Report the malaria status of this cell.
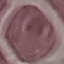
Uninfected.

{
  "stain": "Giemsa",
  "capture": "smartphone through the microscope eyepiece",
  "image_type": "cell patch, automatically extracted from a larger field of view and resized to 64 × 64 pixels",
  "preparation": "thin blood smear"
}